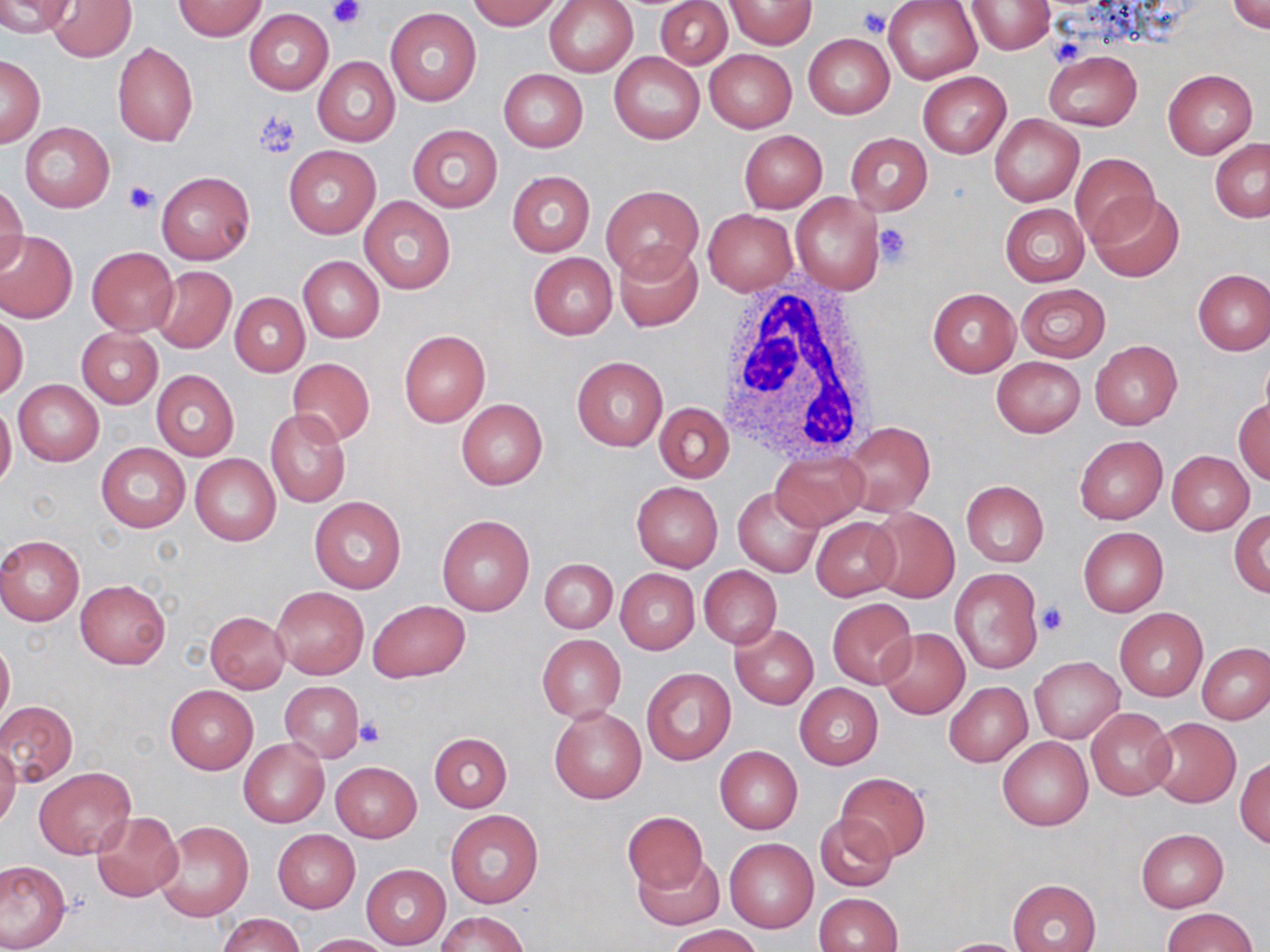

slide-level diagnosis = negative for blood parasites
magnification = 1000x
modality = light microscopy
preparation = thin blood film
field of view = single
uninfected red blood cell locations = approximate bounding boxes as (x1, y1, x2, y2) in pixels: (0, 0, 75, 37), (466, 0, 563, 30), (544, 0, 639, 77), (727, 0, 816, 49), (46, 1, 136, 62), (172, 1, 267, 40), (656, 1, 732, 69), (884, 1, 982, 83), (966, 1, 1053, 55), (1228, 1, 1270, 35), (385, 8, 480, 106), (243, 9, 332, 95), (803, 32, 895, 119), (113, 41, 198, 147), (704, 49, 796, 132), (1043, 50, 1141, 132), (610, 52, 704, 143), (0, 55, 44, 147), (312, 55, 400, 147), (499, 69, 588, 152), (1162, 69, 1256, 159), (918, 71, 1011, 158), (990, 115, 1083, 207), (20, 122, 114, 212), (407, 124, 502, 213), (739, 130, 827, 212), (845, 132, 933, 216), (1210, 138, 1270, 223), (285, 145, 380, 237), (1071, 153, 1158, 242), (156, 171, 255, 264), (507, 171, 595, 256), (1, 183, 27, 276), (601, 184, 703, 281), (1090, 192, 1185, 281), (792, 194, 884, 293), (359, 196, 456, 294), (1001, 204, 1088, 286), (704, 209, 796, 295), (0, 231, 77, 325), (614, 241, 704, 331), (87, 245, 178, 336), (528, 252, 617, 340), (298, 256, 385, 343), (151, 266, 236, 352), (1193, 269, 1270, 355), (1015, 283, 1111, 361), (927, 288, 1020, 377), (229, 293, 309, 376), (0, 313, 26, 401), (76, 328, 162, 408), (398, 330, 490, 426), (1090, 341, 1182, 429), (572, 356, 667, 451), (287, 357, 374, 447), (991, 357, 1085, 437), (151, 370, 238, 462), (14, 379, 102, 466), (1234, 398, 1270, 484), (456, 399, 548, 491), (0, 401, 16, 490), (654, 402, 733, 482), (265, 409, 351, 508), (843, 422, 935, 518), (1074, 435, 1167, 524), (96, 442, 190, 532), (770, 449, 869, 532), (1166, 451, 1253, 536), (190, 454, 280, 546), (961, 480, 1049, 567), (631, 482, 723, 572), (734, 487, 824, 578), (309, 495, 407, 594), (866, 507, 960, 604), (1230, 511, 1270, 596), (435, 515, 535, 617), (812, 517, 901, 600), (1078, 527, 1168, 616), (0, 534, 84, 626), (539, 558, 617, 634), (698, 566, 782, 648), (614, 568, 700, 654), (950, 568, 1042, 674), (76, 579, 170, 669), (272, 587, 368, 678), (827, 598, 917, 690), (368, 599, 470, 682), (1115, 608, 1207, 701), (205, 612, 290, 694), (730, 624, 819, 708), (878, 627, 970, 719), (536, 634, 626, 722), (0, 635, 13, 730), (1198, 644, 1270, 725), (1030, 658, 1123, 742), (641, 668, 737, 766), (279, 681, 363, 763), (945, 681, 1031, 766), (794, 684, 883, 769), (164, 685, 257, 775), (0, 701, 77, 786), (549, 705, 647, 804), (1086, 708, 1176, 801), (1148, 717, 1241, 807), (429, 733, 512, 812), (997, 735, 1093, 830), (239, 740, 328, 826), (0, 743, 20, 830), (714, 745, 803, 834), (1235, 756, 1269, 849), (330, 762, 421, 842), (34, 766, 136, 860), (835, 773, 930, 861), (446, 810, 543, 908), (93, 811, 183, 901), (621, 812, 709, 894), (814, 813, 897, 892), (154, 820, 254, 923), (1135, 828, 1229, 912), (273, 830, 360, 913), (724, 838, 819, 933), (633, 852, 724, 930), (0, 861, 69, 950), (361, 864, 451, 949), (1008, 879, 1101, 952), (814, 893, 902, 952), (1163, 908, 1256, 952), (435, 912, 530, 952), (216, 913, 306, 952), (669, 925, 762, 952), (302, 933, 393, 951), (936, 938, 1035, 952)
image size = 1270×952 pixels
white blood cell locations = approximate bounding boxes as (x1, y1, x2, y2) in pixels: (712, 279, 878, 463)
stain = May-Grünwald-Giemsa
platelet locations = approximate bounding boxes as (x1, y1, x2, y2) in pixels: (327, 1, 364, 27), (857, 8, 890, 36), (1051, 36, 1085, 65), (253, 111, 301, 156), (121, 180, 159, 215), (874, 222, 913, 266), (1038, 602, 1068, 636), (354, 718, 385, 748)